Name the parasite shown.
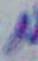
This is Toxoplasma gondii.

modality = micrograph
magnification = 1000x